Look for Plasmodium parasites.
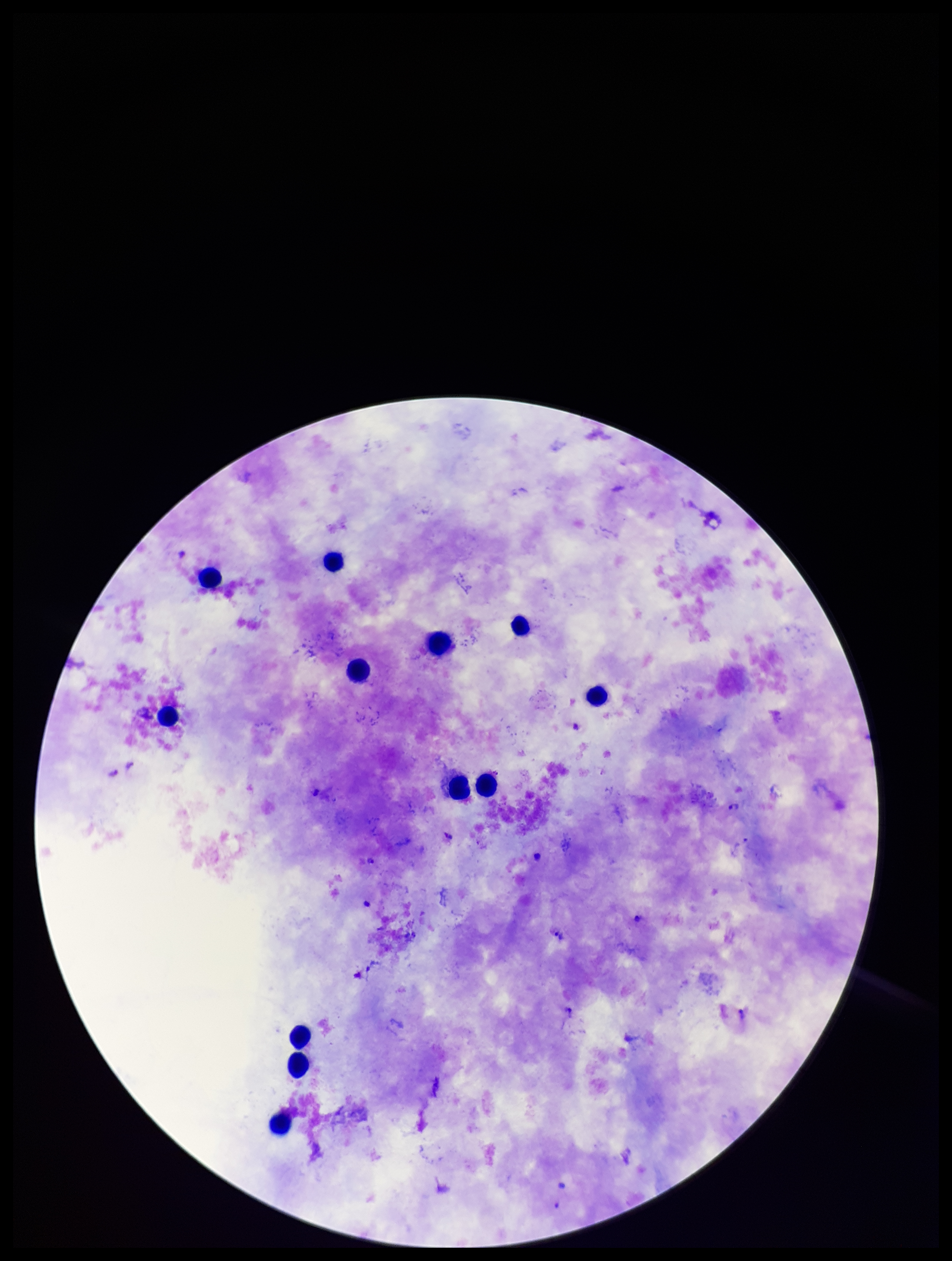

Detected.

{
  "species_reported_for_this_patient": "Plasmodium falciparum",
  "patient_malaria_status": "positive",
  "leukocyte_count": 12,
  "image_size": "952×1261 pixels",
  "parasite_count": 5,
  "field_of_view": "one from this slide",
  "capture": "smartphone photograph through the microscope eyepiece",
  "stain": "Giemsa",
  "preparation": "thick smear"
}